State the preparation type.
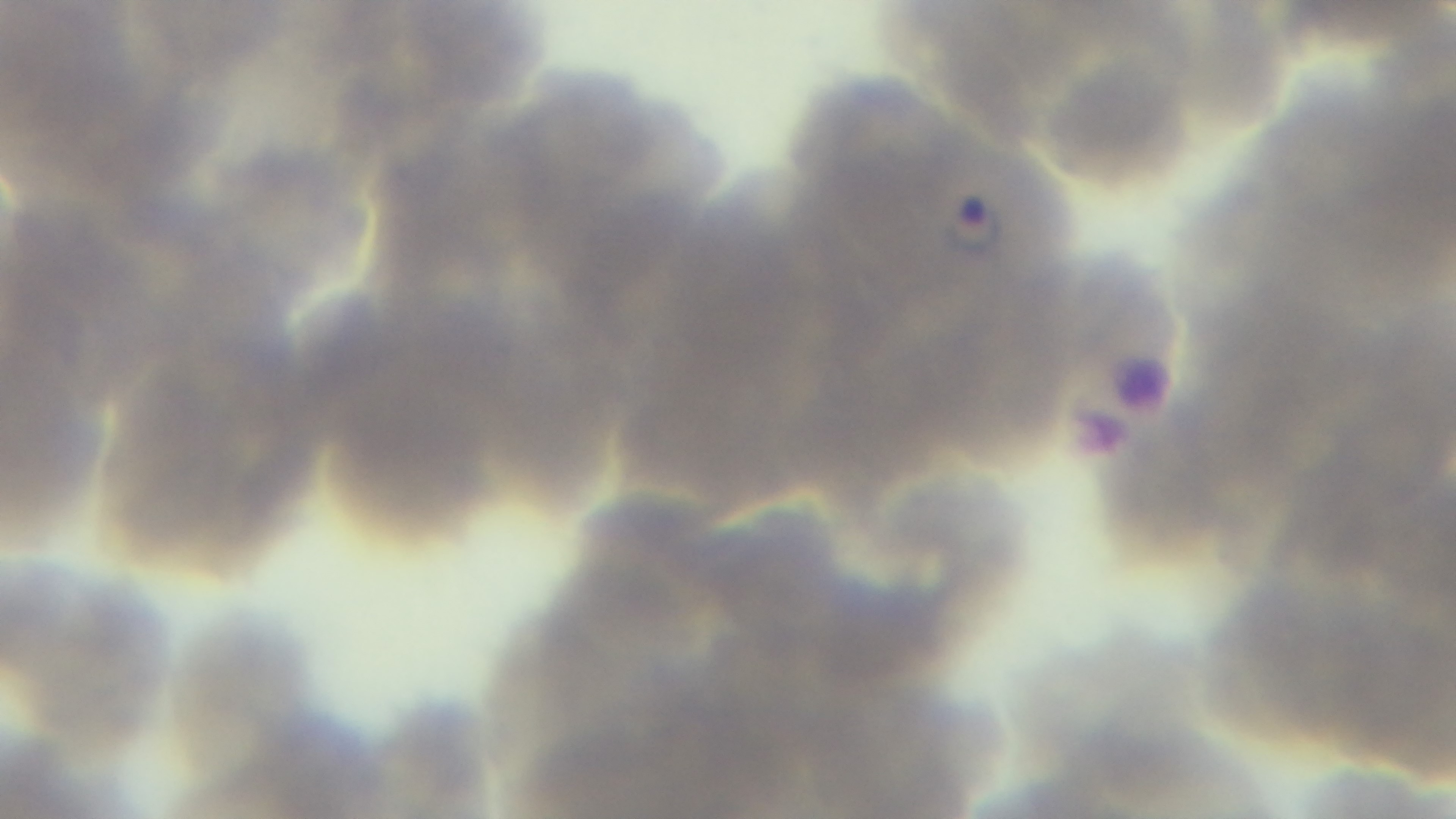

Thin.

modality = light microscopy
objective = 100x oil immersion
field of view = single
capture = mounted 4K digital camera
malaria status = infected
stain = Giemsa